Assess this cell for malaria.
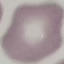

Uninfected.

stain: Giemsa
image_type: cell patch, automatically extracted from a larger field of view and resized to 64 × 64 pixels
preparation: thin smear
capture: smartphone through the microscope eyepiece